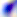
Toxoplasma gondii is shown. Micrograph. Captured at 400x magnification.